Assess this cell for malaria.
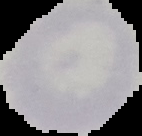

Uninfected.

Summary:
  - Preparation: thin blood smear
  - Image type: cell region segmented out of the field of view; surrounding area masked to black
  - Image size: 142×136 pixels